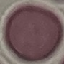
malaria_status: uninfected
capture: smartphone camera at the microscope eyepiece
preparation: thin blood smear
image_type: cell patch, automatically extracted from a larger field of view and resized to 64 × 64 pixels
stain: Giemsa